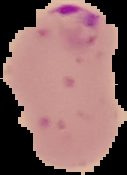

preparation = thin blood film
image size = 127×175 pixels
image type = segmented cell region on a black background
result = malaria parasites detected